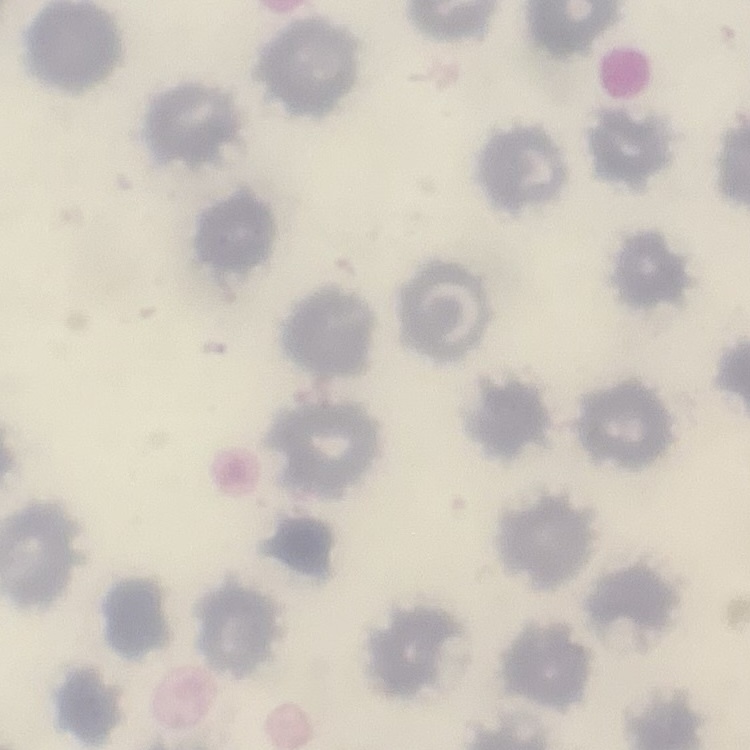

{
  "red_blood_cell_morphology": "no rouleaux formation",
  "image_type": "square crop of a larger photomicrograph",
  "preparation": "thin blood film",
  "stain": "Field's or Giemsa"
}